State which cell type is depicted.
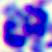
A leukocyte.

magnification = 400x
modality = photomicrograph